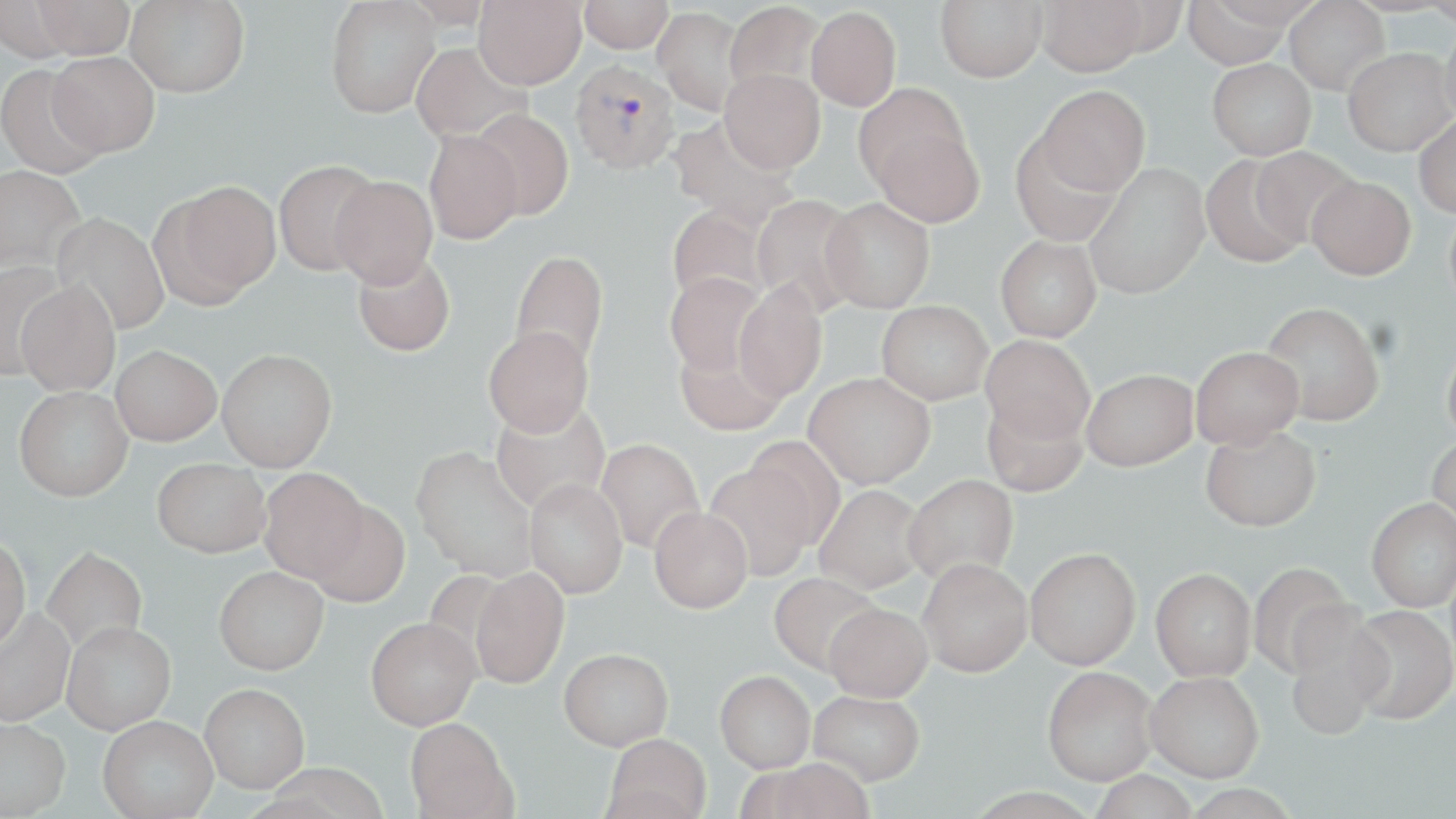

Approximate bounding boxes as named x1/y1/x2/y2 corners in pixels. Plasmodium vivax-infected red blood cell locations: (x1=570, y1=58, x2=680, y2=174). Uninfected red blood cell locations: (x1=31, y1=0, x2=136, y2=59), (x1=125, y1=0, x2=250, y2=98), (x1=325, y1=0, x2=442, y2=117), (x1=474, y1=0, x2=586, y2=89), (x1=579, y1=0, x2=673, y2=53), (x1=935, y1=0, x2=1047, y2=82), (x1=1036, y1=0, x2=1148, y2=75), (x1=1284, y1=0, x2=1390, y2=94), (x1=0, y1=1, x2=77, y2=63), (x1=1179, y1=1, x2=1302, y2=68), (x1=724, y1=2, x2=824, y2=97), (x1=653, y1=7, x2=747, y2=117), (x1=806, y1=7, x2=900, y2=110), (x1=1440, y1=22, x2=1456, y2=126), (x1=409, y1=42, x2=531, y2=143), (x1=1342, y1=47, x2=1454, y2=156), (x1=48, y1=52, x2=159, y2=157), (x1=1207, y1=58, x2=1316, y2=160), (x1=0, y1=62, x2=107, y2=179), (x1=719, y1=68, x2=825, y2=174), (x1=1037, y1=85, x2=1150, y2=196), (x1=470, y1=109, x2=574, y2=221), (x1=1414, y1=115, x2=1456, y2=218), (x1=667, y1=116, x2=799, y2=231), (x1=871, y1=121, x2=984, y2=228), (x1=423, y1=129, x2=523, y2=245), (x1=1011, y1=132, x2=1122, y2=247), (x1=1251, y1=147, x2=1358, y2=246), (x1=1200, y1=154, x2=1308, y2=267), (x1=273, y1=159, x2=382, y2=277), (x1=1084, y1=163, x2=1210, y2=300), (x1=0, y1=164, x2=86, y2=274), (x1=330, y1=175, x2=438, y2=288), (x1=1307, y1=176, x2=1415, y2=280), (x1=161, y1=180, x2=282, y2=302), (x1=751, y1=194, x2=864, y2=316), (x1=820, y1=197, x2=935, y2=312), (x1=1445, y1=203, x2=1456, y2=312), (x1=667, y1=205, x2=770, y2=307), (x1=52, y1=212, x2=170, y2=337), (x1=995, y1=235, x2=1101, y2=342), (x1=510, y1=250, x2=609, y2=370), (x1=351, y1=251, x2=455, y2=357), (x1=0, y1=260, x2=68, y2=383), (x1=664, y1=271, x2=768, y2=378), (x1=16, y1=279, x2=120, y2=397), (x1=733, y1=281, x2=827, y2=402), (x1=877, y1=300, x2=993, y2=404), (x1=1260, y1=301, x2=1384, y2=427), (x1=483, y1=326, x2=594, y2=437), (x1=981, y1=335, x2=1095, y2=444), (x1=1442, y1=338, x2=1456, y2=448), (x1=674, y1=339, x2=786, y2=437), (x1=111, y1=345, x2=221, y2=446), (x1=1190, y1=346, x2=1303, y2=449), (x1=217, y1=348, x2=337, y2=472), (x1=1082, y1=369, x2=1198, y2=471), (x1=804, y1=372, x2=935, y2=488), (x1=14, y1=386, x2=133, y2=501), (x1=981, y1=395, x2=1088, y2=497), (x1=489, y1=399, x2=612, y2=514), (x1=1201, y1=425, x2=1321, y2=532), (x1=1427, y1=434, x2=1456, y2=537), (x1=742, y1=436, x2=845, y2=547), (x1=595, y1=438, x2=705, y2=555), (x1=411, y1=446, x2=539, y2=581), (x1=152, y1=457, x2=269, y2=557), (x1=703, y1=463, x2=818, y2=581), (x1=259, y1=468, x2=368, y2=582), (x1=903, y1=473, x2=1018, y2=584), (x1=524, y1=478, x2=628, y2=599), (x1=814, y1=484, x2=929, y2=594), (x1=1366, y1=497, x2=1456, y2=611), (x1=309, y1=501, x2=409, y2=608), (x1=648, y1=506, x2=753, y2=613), (x1=0, y1=536, x2=30, y2=653), (x1=41, y1=546, x2=148, y2=655), (x1=1025, y1=547, x2=1140, y2=669), (x1=918, y1=558, x2=1033, y2=676), (x1=1247, y1=562, x2=1355, y2=679), (x1=214, y1=566, x2=329, y2=675), (x1=469, y1=567, x2=569, y2=689), (x1=1150, y1=567, x2=1256, y2=681), (x1=768, y1=572, x2=883, y2=675), (x1=823, y1=602, x2=933, y2=702), (x1=1348, y1=604, x2=1456, y2=725), (x1=0, y1=606, x2=75, y2=727), (x1=1283, y1=613, x2=1390, y2=740), (x1=366, y1=617, x2=481, y2=730), (x1=61, y1=621, x2=176, y2=734), (x1=559, y1=647, x2=674, y2=750), (x1=1042, y1=666, x2=1157, y2=785), (x1=715, y1=670, x2=816, y2=772), (x1=1145, y1=671, x2=1264, y2=782), (x1=200, y1=682, x2=310, y2=793), (x1=809, y1=689, x2=924, y2=785), (x1=97, y1=715, x2=218, y2=818), (x1=0, y1=716, x2=71, y2=818), (x1=405, y1=717, x2=514, y2=819), (x1=603, y1=733, x2=711, y2=819), (x1=757, y1=757, x2=879, y2=819). Slide-level diagnosis: Plasmodium vivax. May-Grünwald-Giemsa stain. One field of a larger specimen. Captured at 1000x magnification. Thin blood smear. Optical microscopy. Image is 1456×819 pixels.